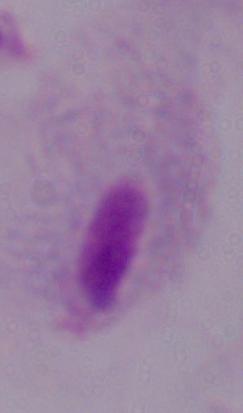

Micrograph. A trichomonad is seen. 1000x magnification.